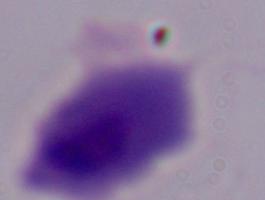
Summary:
  - Identification: trichomonad
  - Magnification: 1000x
  - Modality: photomicrograph